Assess this cell for malaria.
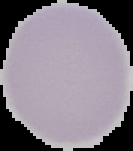
Uninfected.

Segmented cell region on a black background. Image is 133×151 pixels. From a thin blood smear.